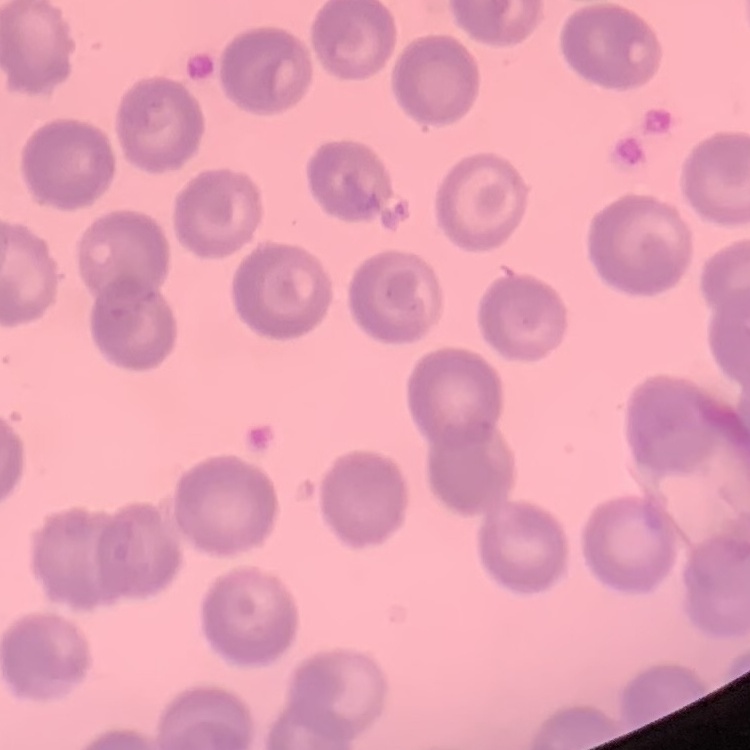

Summary:
  - Erythrocyte morphology: no rouleaux formation
  - Image type: one tile cut from a larger photomicrograph
  - Stain: Field's or Giemsa
  - Preparation: thin blood smear